Outline every Plasmodium parasite.
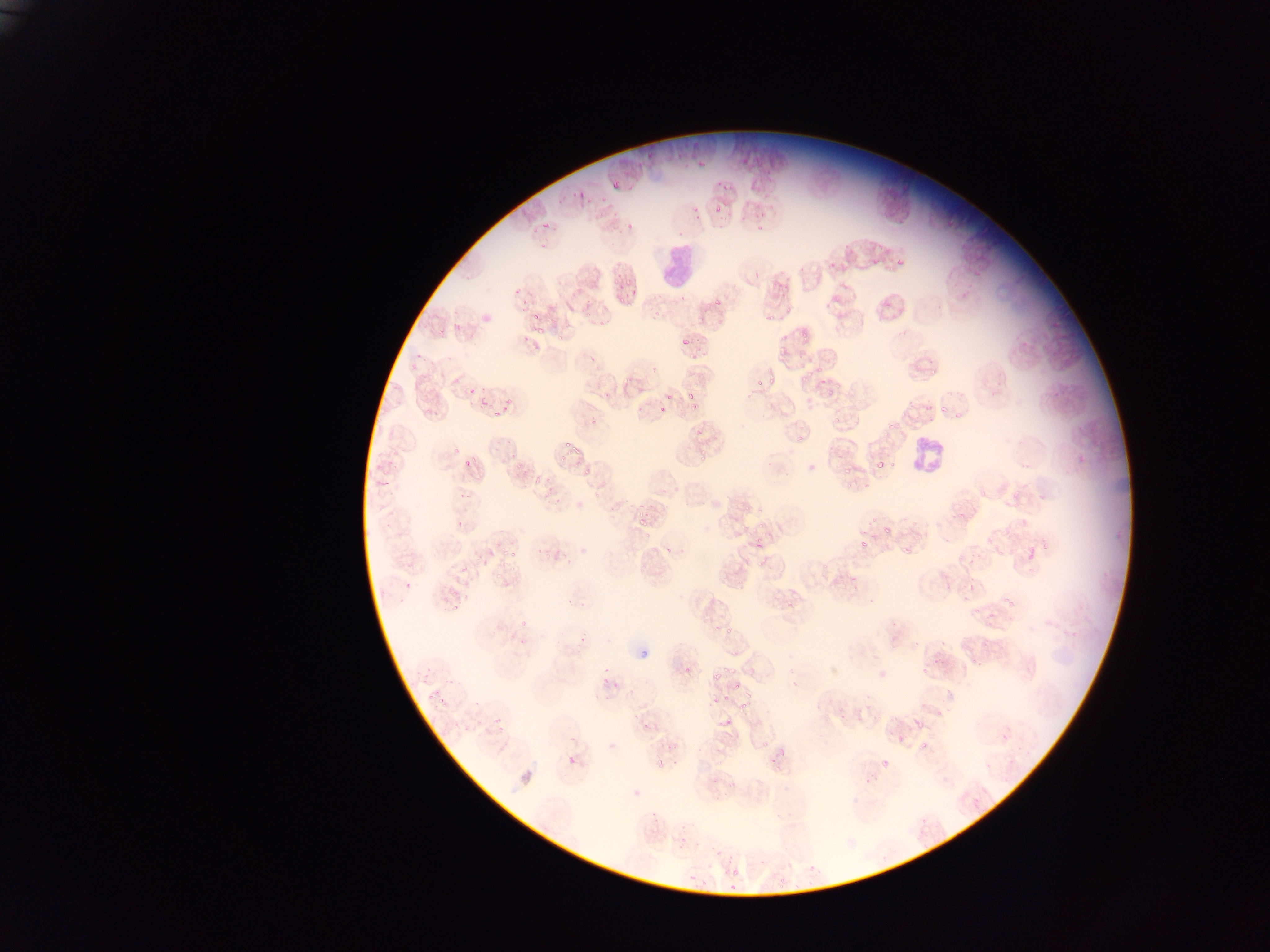

Approximate bounding boxes as (left, top, right, bottom) in pixels.
Plasmodium parasites: (698, 153, 707, 167), (718, 177, 731, 192), (610, 178, 622, 189), (579, 186, 587, 201), (560, 191, 572, 203), (597, 192, 606, 203), (692, 201, 705, 223), (712, 203, 721, 214), (738, 208, 749, 223), (543, 216, 553, 228), (754, 219, 764, 230), (624, 221, 632, 227), (530, 227, 538, 233), (541, 237, 552, 251), (844, 252, 853, 264), (896, 252, 906, 266), (751, 268, 766, 282), (613, 272, 622, 285), (514, 279, 525, 294), (624, 279, 633, 285), (617, 282, 625, 290), (627, 289, 639, 296), (678, 292, 689, 303), (520, 294, 531, 304), (714, 296, 723, 307), (618, 298, 625, 308), (626, 301, 634, 307), (784, 305, 793, 317), (524, 309, 536, 320), (580, 312, 590, 319), (765, 313, 774, 324), (436, 318, 453, 333), (536, 322, 549, 336), (597, 322, 605, 327), (796, 325, 808, 337), (521, 330, 532, 341), (680, 332, 691, 343), (552, 337, 565, 345), (798, 338, 807, 349), (778, 346, 786, 357), (413, 349, 427, 358), (691, 355, 701, 362), (409, 357, 423, 372), (928, 361, 939, 374), (763, 363, 773, 375), (815, 367, 823, 374), (801, 371, 812, 382), (767, 375, 776, 386), (818, 378, 828, 386), (833, 379, 841, 390), (469, 385, 477, 395), (685, 388, 694, 403), (825, 389, 834, 400), (665, 393, 673, 400), (479, 394, 487, 406), (504, 397, 515, 411), (925, 397, 936, 413), (690, 402, 698, 409), (658, 403, 667, 415), (939, 404, 949, 415), (423, 408, 432, 415), (491, 408, 500, 416), (952, 412, 963, 421), (833, 415, 841, 423), (590, 418, 600, 426), (888, 420, 896, 431), (691, 428, 704, 439), (495, 430, 512, 447), (566, 433, 570, 447), (796, 433, 803, 444), (573, 445, 585, 454), (451, 446, 467, 456), (559, 449, 568, 462), (696, 449, 708, 462), (511, 452, 520, 458), (463, 455, 477, 466), (876, 457, 887, 468), (583, 463, 594, 474), (842, 463, 851, 476), (381, 475, 394, 486), (545, 475, 553, 488), (533, 478, 541, 485), (845, 478, 853, 491), (860, 482, 870, 490), (451, 492, 465, 503), (542, 495, 550, 503), (741, 505, 749, 516), (752, 505, 764, 513), (954, 512, 963, 520), (634, 513, 648, 526), (758, 516, 770, 528), (867, 516, 876, 527), (456, 521, 466, 527), (881, 523, 890, 532), (643, 529, 654, 539), (755, 536, 764, 550), (860, 538, 865, 547), (899, 541, 910, 556), (501, 548, 508, 556), (663, 549, 673, 554), (512, 552, 517, 560), (956, 558, 964, 566), (565, 559, 572, 569), (754, 562, 767, 573), (944, 581, 953, 589), (402, 583, 413, 589), (451, 591, 462, 598), (1002, 591, 1013, 605), (566, 593, 572, 605), (973, 600, 984, 617), (448, 601, 460, 612), (988, 613, 998, 620), (520, 619, 529, 627), (726, 626, 735, 638), (579, 630, 590, 644), (515, 640, 523, 646), (638, 646, 653, 661), (603, 656, 609, 673), (682, 663, 694, 674), (921, 667, 928, 678), (420, 671, 429, 681), (713, 671, 725, 679), (596, 677, 610, 688), (613, 681, 619, 690), (445, 682, 455, 685), (433, 685, 438, 697), (733, 685, 742, 690), (744, 689, 758, 700), (425, 691, 431, 699), (712, 694, 722, 704), (722, 695, 732, 700), (437, 698, 445, 705), (737, 703, 748, 713), (935, 706, 946, 716), (493, 716, 503, 728), (722, 717, 730, 727), (451, 718, 462, 729), (640, 721, 649, 732), (916, 723, 924, 732), (894, 737, 902, 748), (915, 737, 929, 754), (756, 740, 770, 751), (567, 754, 579, 767), (675, 756, 682, 765), (654, 760, 662, 768), (881, 763, 891, 770), (863, 778, 873, 791), (966, 795, 984, 813), (678, 838, 687, 847), (728, 869, 738, 875), (690, 873, 696, 882), (778, 873, 794, 887), (729, 877, 737, 891), (700, 879, 708, 890) | approximate (x, y) pixel centers of objects too small to bound: (745, 160), (830, 264), (758, 384), (893, 463), (519, 468), (539, 549), (464, 567), (582, 601), (476, 702), (667, 746), (781, 753).

Summary:
  - Leukocyte locations: (652, 239, 703, 294), (906, 431, 952, 483)
  - Country: Ghana
  - Image size: 1270×952 pixels
  - Preparation: thin blood film
  - Capture: mobile-phone photograph through a microscope
  - Field of view: single